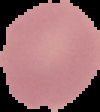
From a thin blood film. Result: no malaria parasites detected. Segmented cell region on a black background. Image is 100×112 pixels.